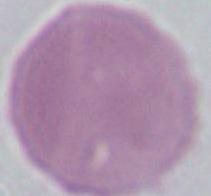

magnification = 1000x
identification = erythrocyte
modality = photomicrograph